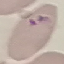

malaria status = parasitized
capture = smartphone camera at the microscope eyepiece
preparation = thin smear
stain = Giemsa
image type = cell patch, automatically extracted from a larger field of view and resized to 64 × 64 pixels